Identify the cell.
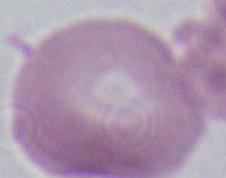
An erythrocyte.

Captured at 1000x magnification. Photomicrograph.